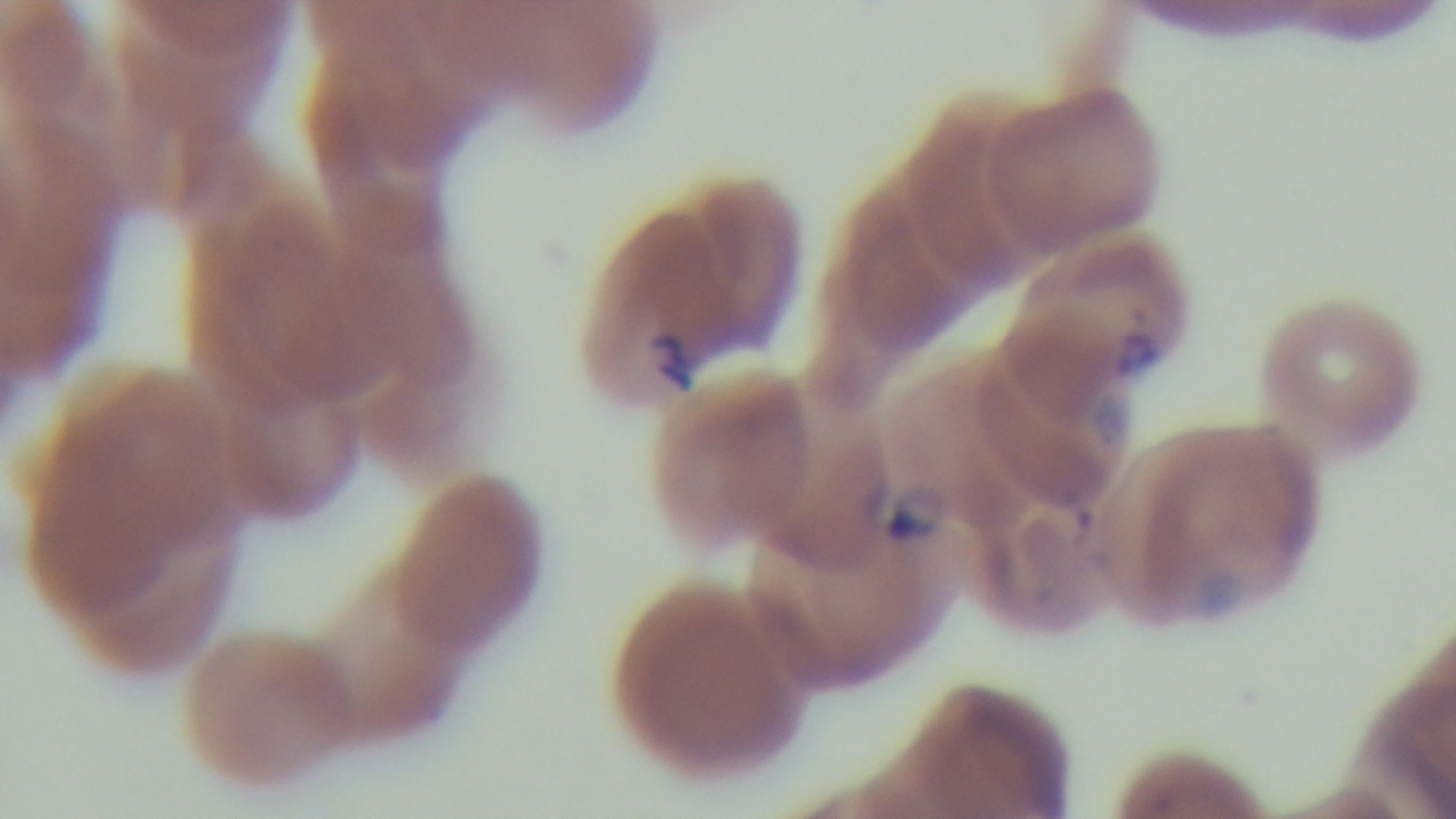
Preparation: thin blood film. Mounted 4K digital camera. Light microscopy. Giemsa-stained. Single field of view. 100x oil-immersion objective. Malaria status: infected.